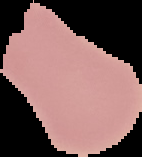
Summary:
  - Preparation: thin blood smear
  - Image type: cell region segmented out of the field of view; surrounding area masked to black
  - Image size: 142×157 pixels
  - Malaria status: uninfected